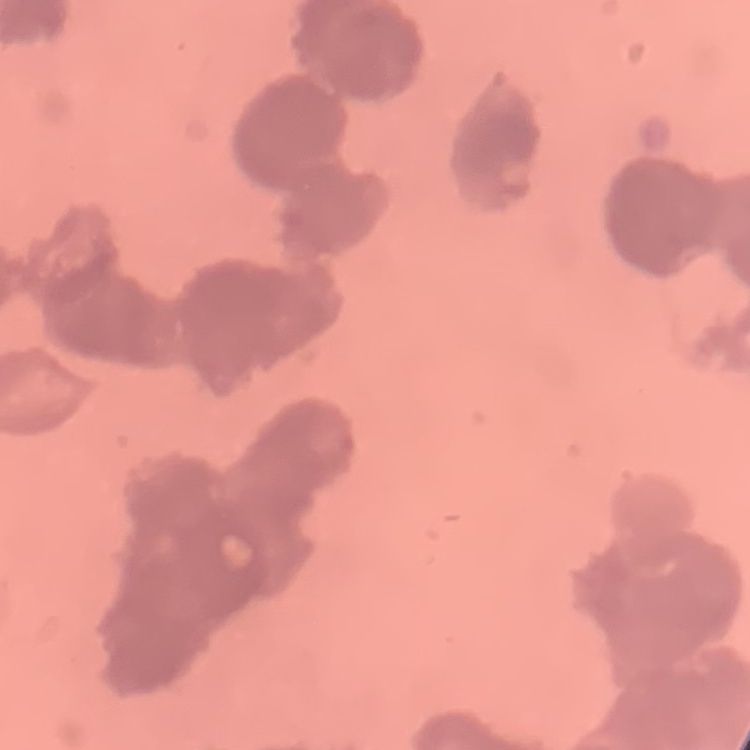
Summary:
  - Red blood cell morphology: rouleaux formation
  - Preparation: thin blood smear
  - Stain: Field's or Giemsa
  - Image type: one tile cut from a larger photomicrograph